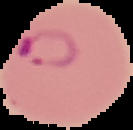

preparation = thin blood smear
malaria status = parasitized
image size = 133×130 pixels
image type = segmented cell region on a black background